Look for Plasmodium parasites.
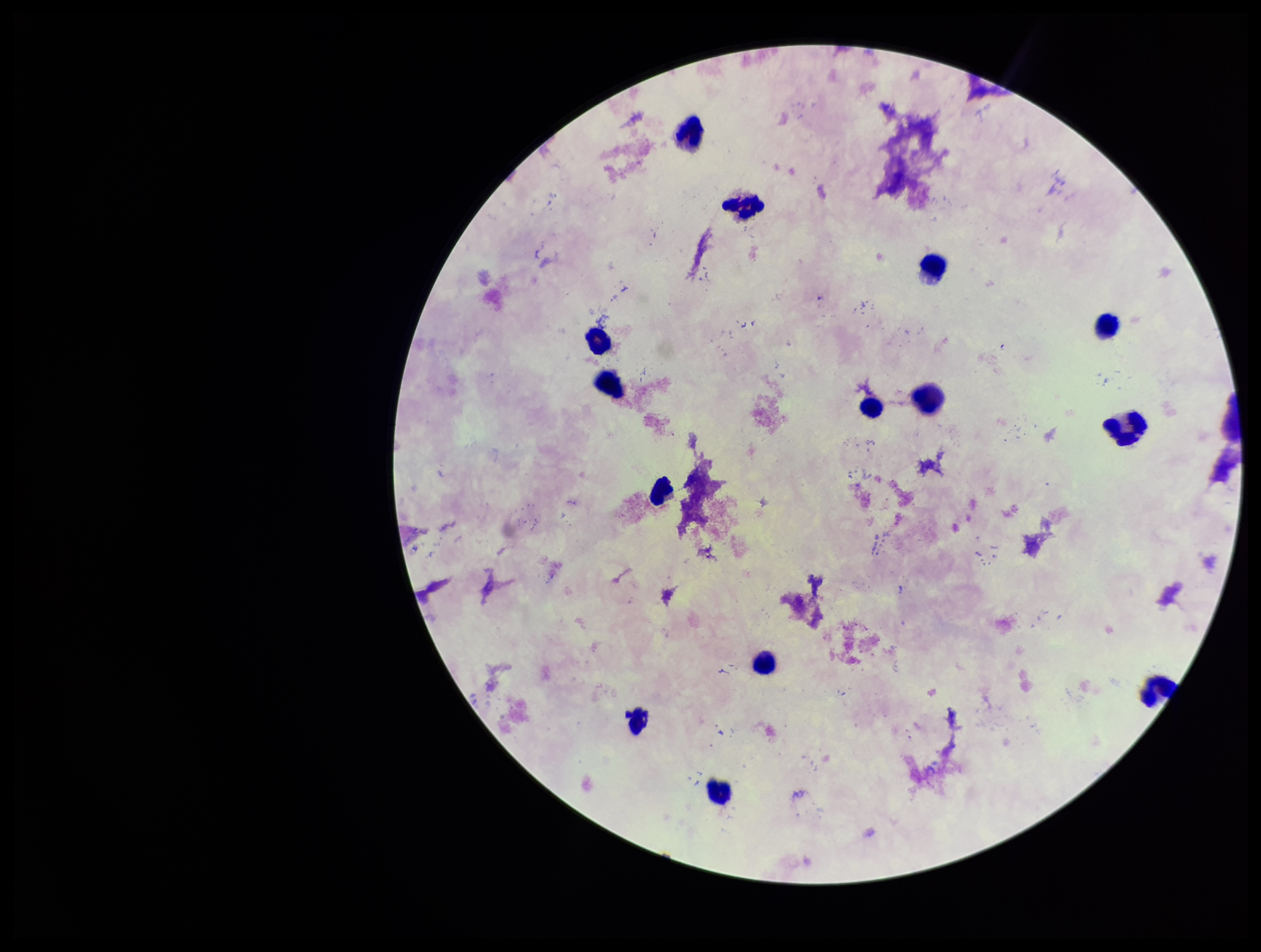

None detected.

Parasite count: 0. One field from this slide. Stained with Giemsa. Image is 1261×952 pixels. Patient malaria status: negative. Leukocyte count: 13. Preparation: thick blood smear. Photographed through the microscope eyepiece with a smartphone camera.